Identify the cell.
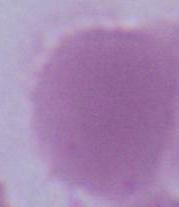
An erythrocyte.

Summary:
  - Modality: photomicrograph
  - Magnification: 1000x